Classify this cell by malaria status.
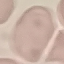

Uninfected.

preparation = thin blood film
stain = Giemsa
image type = automatically extracted cell patch, resized to 64 × 64 pixels
capture = smartphone through the microscope eyepiece